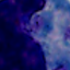

1000x magnification. Photomicrograph. A leukocyte is shown.